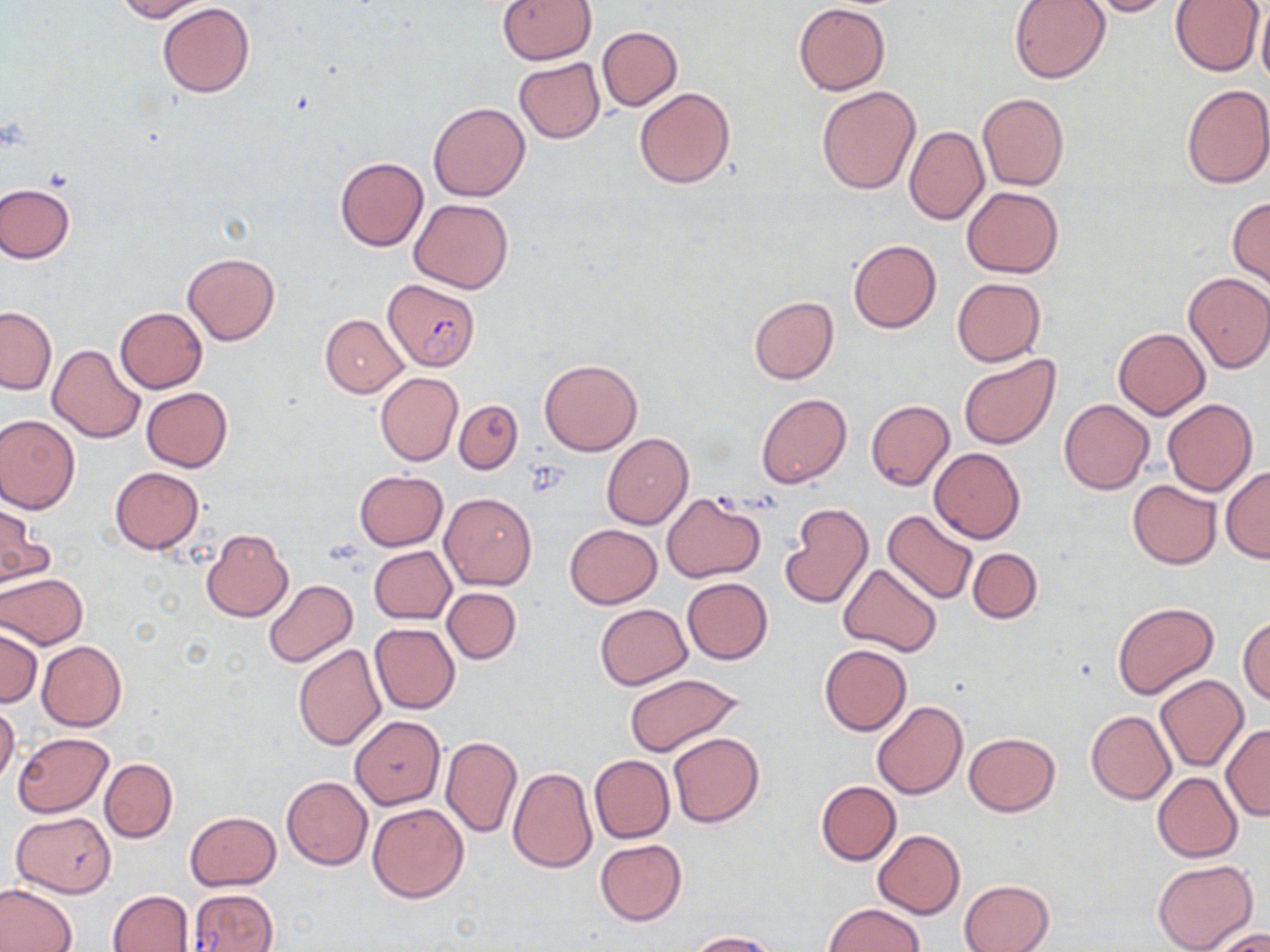

Summary:
  - Coordinate format: approximate bounding boxes as (x1, y1, x2, y2) in pixels
  - Plasmodium falciparum-infected red blood cell locations: (383, 278, 480, 371), (188, 889, 278, 952)
  - Uninfected red blood cell locations: (115, 0, 210, 21), (498, 0, 596, 64), (1008, 0, 1111, 84), (1081, 0, 1181, 17), (1169, 0, 1265, 76), (793, 2, 890, 95), (157, 3, 254, 98), (1256, 6, 1270, 88), (597, 25, 682, 111), (513, 58, 605, 143), (1182, 83, 1270, 189), (816, 85, 920, 193), (634, 87, 737, 189), (977, 92, 1068, 191), (429, 103, 530, 202), (904, 126, 988, 225), (335, 156, 428, 250), (0, 183, 75, 262), (961, 186, 1064, 279), (1227, 197, 1270, 289), (409, 198, 514, 294), (849, 239, 941, 333), (182, 252, 279, 345), (1183, 272, 1270, 372), (952, 277, 1046, 365), (749, 295, 839, 384), (0, 307, 56, 394), (115, 307, 207, 393), (320, 314, 409, 397), (1113, 328, 1210, 420), (47, 343, 144, 443), (959, 354, 1061, 450), (539, 360, 643, 455), (375, 371, 463, 466), (141, 387, 232, 472), (756, 393, 851, 488), (1162, 398, 1257, 496), (454, 400, 523, 473), (866, 400, 954, 492), (1059, 400, 1154, 495), (0, 414, 81, 514), (602, 433, 692, 529), (929, 448, 1026, 543), (1220, 466, 1270, 562), (110, 467, 204, 554), (354, 471, 448, 550), (1128, 479, 1221, 568), (441, 493, 536, 589), (662, 494, 765, 583), (780, 503, 874, 609), (0, 505, 51, 586), (882, 510, 979, 606), (564, 524, 661, 609), (200, 528, 294, 623), (370, 545, 456, 623), (967, 548, 1042, 623), (839, 562, 941, 657), (0, 573, 88, 648), (682, 577, 772, 664), (263, 579, 358, 668), (442, 587, 520, 664), (1111, 601, 1218, 699), (594, 604, 692, 689), (1238, 616, 1270, 705), (370, 624, 460, 715), (0, 627, 42, 707), (37, 640, 127, 731), (293, 643, 386, 751), (819, 644, 911, 735), (623, 672, 745, 757), (1155, 674, 1248, 772), (871, 701, 966, 799), (0, 703, 20, 785), (1085, 710, 1176, 804), (350, 716, 445, 808), (1221, 724, 1270, 820), (13, 732, 112, 817), (668, 732, 763, 828), (963, 732, 1060, 816), (441, 737, 523, 838), (589, 754, 674, 843), (100, 758, 177, 843), (507, 767, 597, 872), (1152, 772, 1243, 862), (281, 776, 372, 869), (816, 780, 901, 865), (367, 802, 470, 903), (184, 811, 280, 890), (10, 812, 115, 897), (873, 830, 964, 918), (595, 839, 686, 926), (1152, 859, 1258, 952), (960, 879, 1053, 952), (0, 882, 77, 952), (107, 890, 195, 952), (822, 903, 925, 952), (1206, 925, 1270, 952), (688, 931, 781, 952)
  - Slide-level diagnosis: Plasmodium falciparum
  - Stain: May-Grünwald-Giemsa
  - Image size: 1270×952 pixels
  - Preparation: thin blood film
  - Modality: optical microscopy
  - Field of view: one of a larger specimen
  - Magnification: 1000x